Assess the morphology of the erythrocytes.
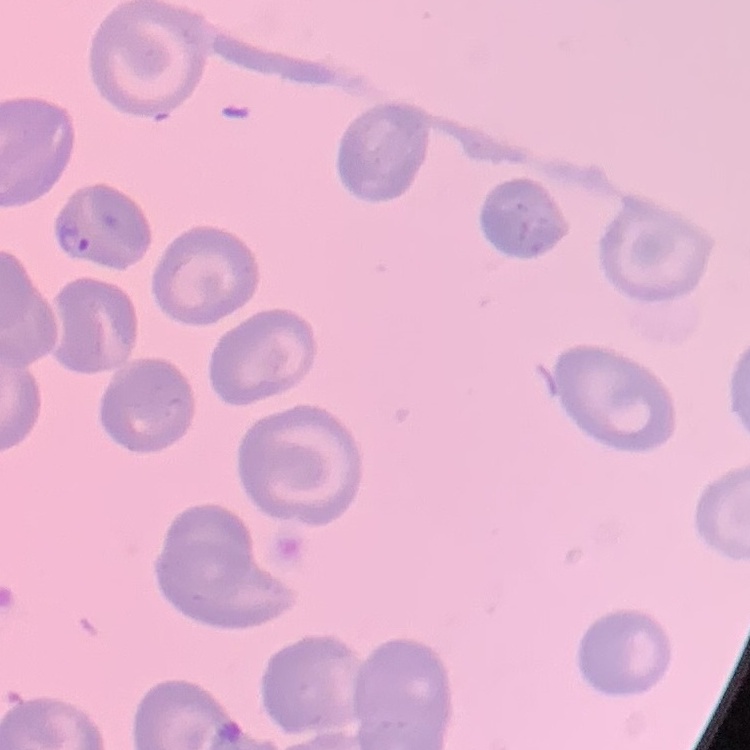
No rouleaux formation.

{
  "preparation": "thin peripheral smear",
  "image_type": "square crop of a larger photomicrograph",
  "stain": "Field's or Giemsa"
}